State which parasite is depicted.
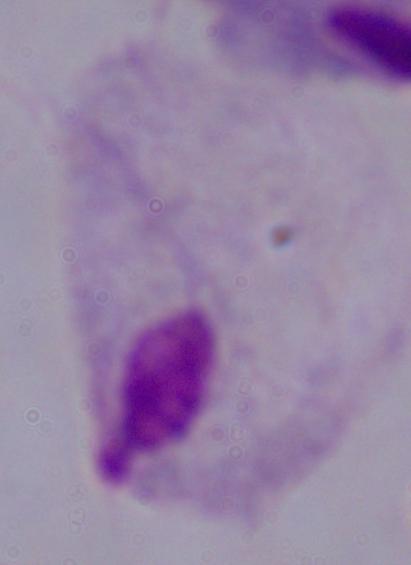

A trichomonad.

Summary:
  - Modality: photomicrograph
  - Magnification: 1000x